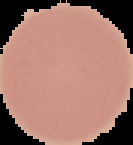 Image is 133×145 pixels. Segmented cell region on a black background. Malaria status: uninfected. From a thin blood smear.